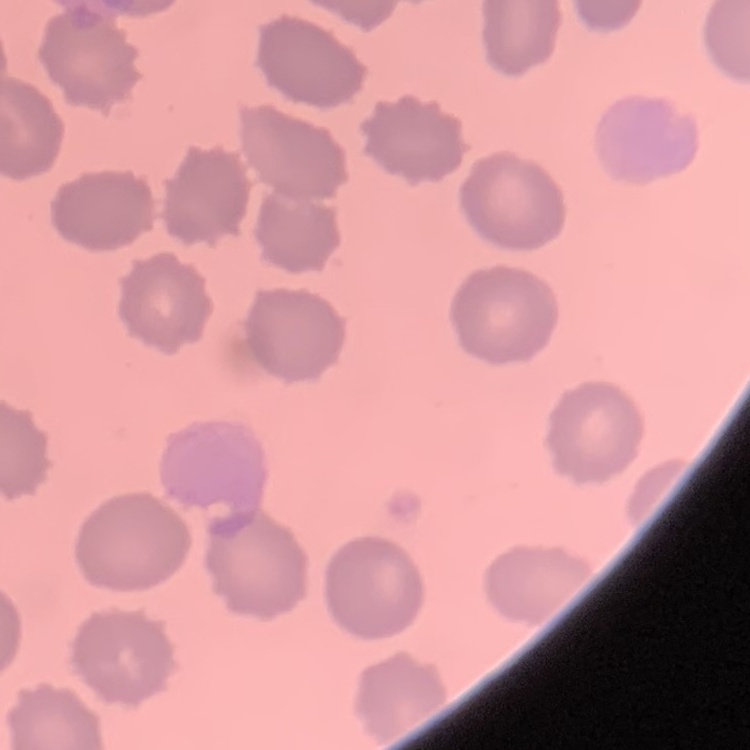
Summary:
  - Red blood cell morphology: no rouleaux formation
  - Preparation: thin peripheral smear
  - Stain: Field's or Giemsa
  - Image type: one tile cut from a larger photomicrograph